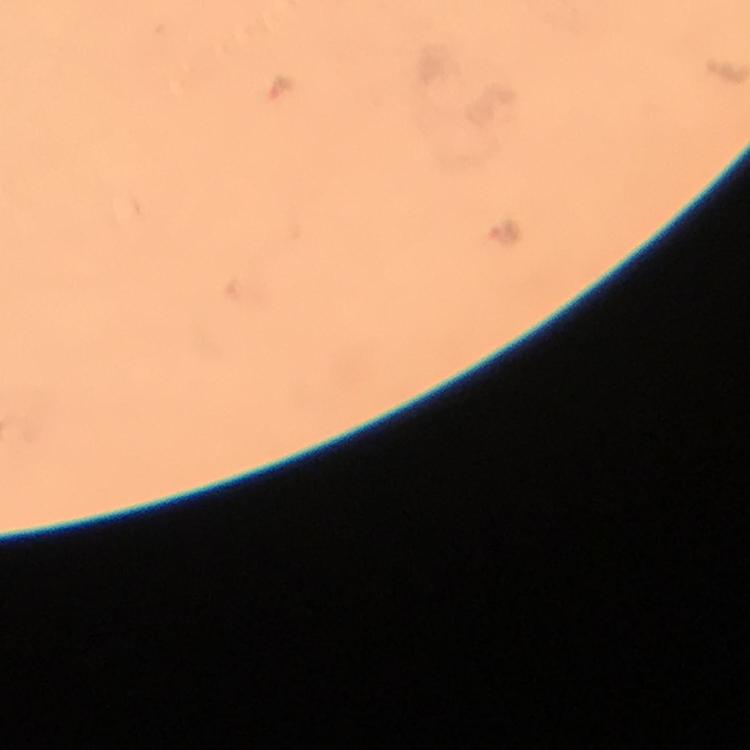

Approximate centers as [x, y] in pixels.
Summary:
  - Malaria parasite locations: [284, 89], [506, 233]
  - Context: from a diagnostic examination for malaria
  - Image size: 750×750 pixels
  - Stain: Giemsa
  - Capture: smartphone mounted on the microscope
  - Immersion oil: applied
  - Preparation: thick smear
  - Cropped from: a single field of view
  - Magnification: 100x